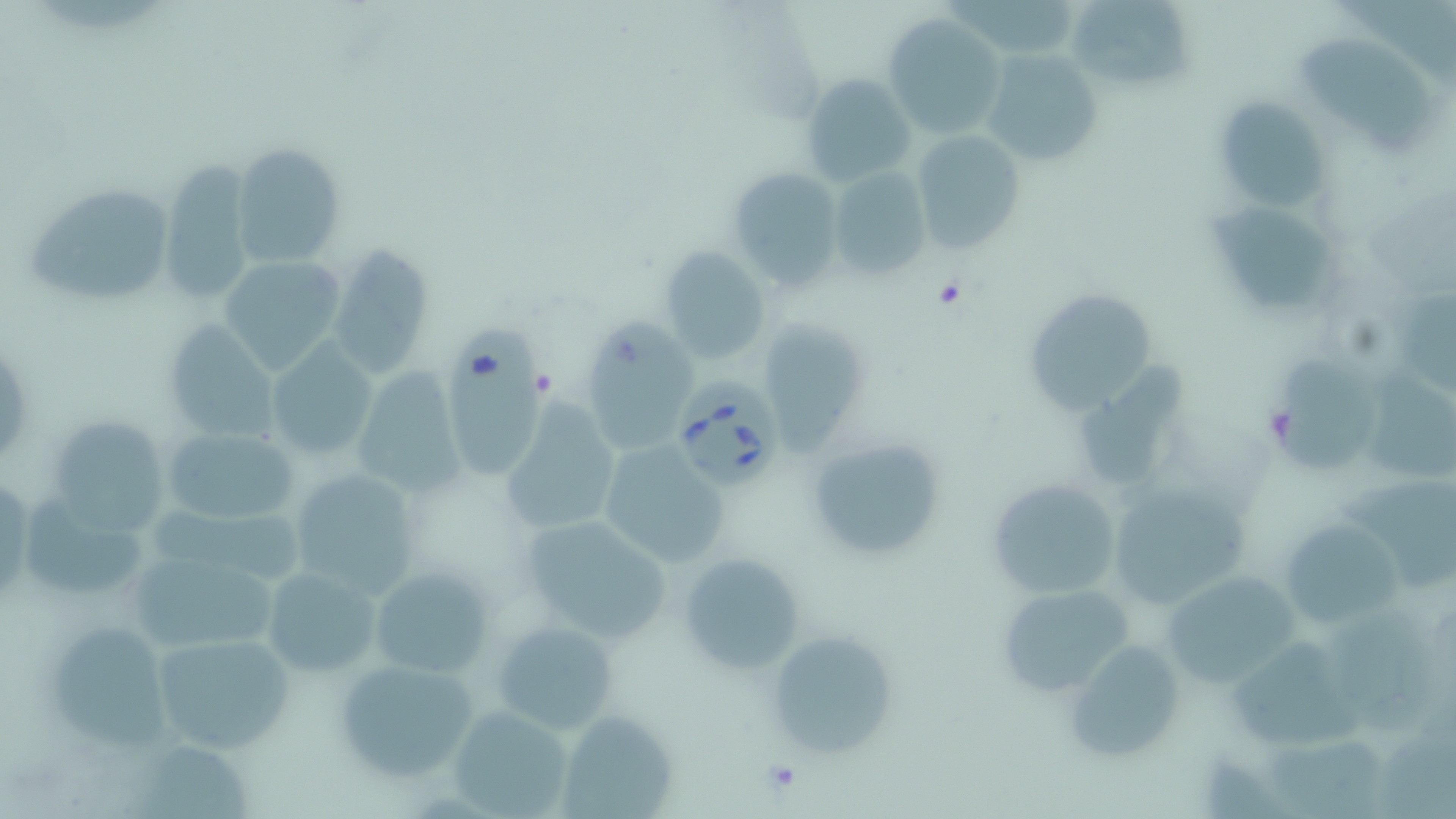

Approximate bounding boxes as (x1, y1, x2, y2) in pixels. Platelet locations: (932, 277, 969, 311), (759, 757, 805, 796). Babesia divergens-infected red blood cell locations: (671, 374, 782, 492). Uninfected red blood cell locations: (1064, 0, 1195, 92), (881, 14, 1005, 139), (1303, 35, 1432, 159), (982, 49, 1101, 167), (802, 72, 916, 191), (1210, 95, 1334, 215), (911, 129, 1026, 257), (229, 142, 344, 269), (158, 162, 258, 306), (727, 167, 844, 292), (828, 168, 933, 281), (20, 182, 177, 310), (1204, 198, 1342, 321), (336, 241, 429, 376), (661, 247, 770, 368), (217, 256, 344, 375), (1020, 282, 1162, 414), (585, 316, 698, 447), (163, 322, 282, 443), (763, 322, 865, 457), (444, 327, 548, 474), (263, 340, 377, 463), (1073, 346, 1193, 499), (1361, 359, 1456, 479), (1273, 360, 1382, 477), (350, 366, 465, 497), (501, 398, 619, 536), (46, 415, 171, 534), (161, 426, 302, 528), (806, 435, 951, 563), (596, 439, 732, 568), (285, 466, 421, 601), (1338, 471, 1456, 592), (0, 474, 32, 604), (986, 477, 1123, 601), (1106, 481, 1251, 606), (146, 495, 308, 587), (24, 496, 150, 600), (1283, 507, 1413, 627), (515, 514, 674, 643), (677, 552, 806, 675), (130, 560, 288, 646), (261, 565, 381, 678), (368, 565, 491, 678), (1160, 569, 1300, 691), (996, 582, 1135, 698), (40, 616, 177, 749), (492, 617, 621, 737), (765, 630, 895, 759), (151, 633, 296, 755), (1234, 635, 1361, 753), (1062, 638, 1187, 766), (331, 655, 483, 785), (447, 705, 575, 818), (557, 709, 677, 818), (1264, 734, 1386, 817). Slide-level diagnosis: Babesia divergens. Thin blood film. Optical microscopy. May-Grünwald-Giemsa-stained preparation. Single field of view. Image is 1456×819 pixels. 1000x magnification.